Mark where platelets are.
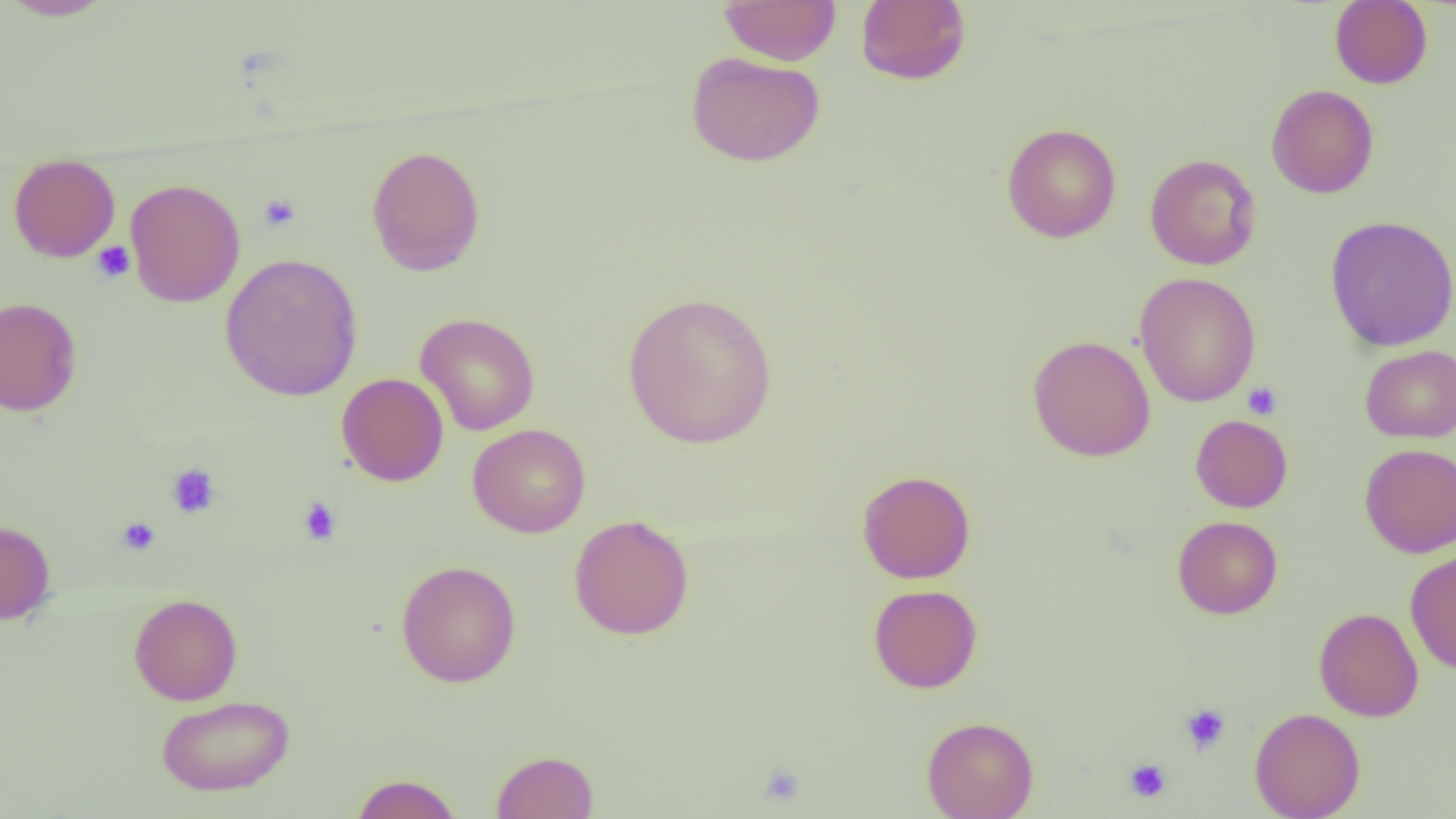

Approximate bounding boxes as (x1, y1, x2, y2) in pixels.
Platelets: (259, 193, 301, 232), (91, 241, 135, 284), (1242, 382, 1282, 420), (166, 464, 220, 518), (298, 497, 342, 544), (116, 517, 160, 555), (1179, 703, 1231, 755), (1123, 758, 1172, 803), (756, 761, 807, 809).

Summary:
  - Uninfected red blood cell locations: (1, 0, 116, 21), (719, 0, 842, 65), (855, 0, 971, 86), (1329, 0, 1433, 89), (685, 51, 825, 167), (1266, 84, 1379, 199), (1001, 122, 1122, 243), (366, 145, 486, 276), (8, 153, 120, 262), (1144, 153, 1262, 270), (125, 178, 245, 307), (1324, 215, 1456, 352), (220, 253, 363, 401), (1134, 272, 1261, 407), (622, 291, 777, 449), (0, 296, 83, 417), (415, 312, 541, 435), (1027, 335, 1155, 461), (1360, 345, 1456, 443), (336, 373, 449, 486), (1190, 414, 1293, 513), (468, 424, 591, 538), (1359, 444, 1456, 557), (857, 469, 976, 584), (568, 514, 695, 640), (1172, 515, 1283, 619), (0, 518, 56, 625), (1405, 548, 1456, 674), (395, 559, 521, 687), (868, 584, 982, 693), (128, 593, 243, 705), (1314, 607, 1424, 722), (156, 694, 295, 797), (1249, 707, 1365, 818), (921, 715, 1038, 819), (490, 749, 599, 818), (350, 773, 464, 818)
  - Slide-level diagnosis: negative for blood parasites
  - Modality: optical microscopy
  - Magnification: 1000x
  - Field of view: one of a larger specimen
  - Preparation: thin blood film
  - Image size: 1456×819 pixels